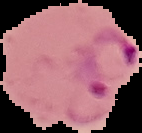

Summary:
  - Image type: segmented cell region on a black background
  - Malaria status: parasitized
  - Image size: 142×133 pixels
  - Preparation: thin blood smear